Classify this cell by malaria status.
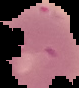

It is uninfected.

{
  "image_size": "79×88 pixels",
  "preparation": "thin blood film",
  "image_type": "cell region segmented out of the field of view; surrounding area masked to black"
}